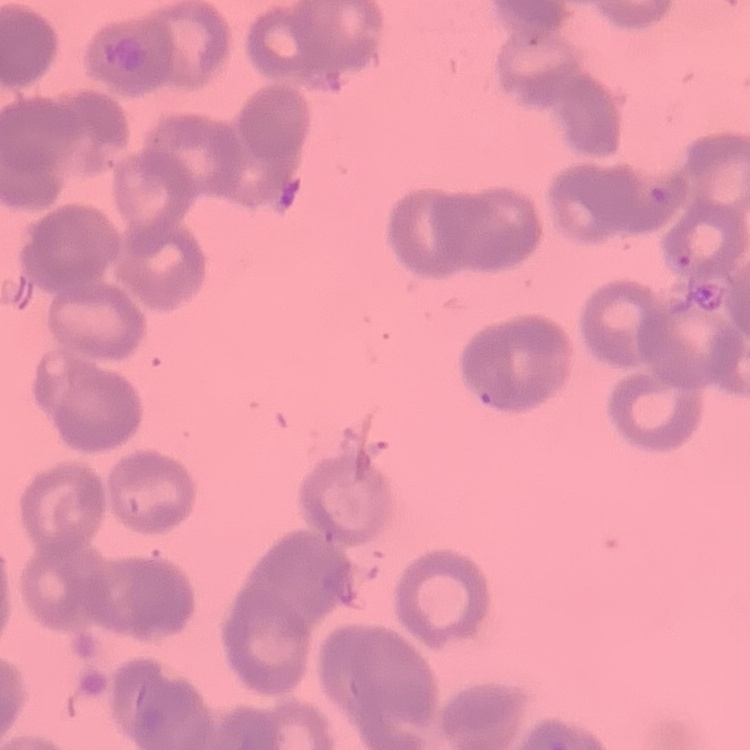

The red blood cells exhibit rouleaux formation. Thin blood smear. Field's or Giemsa stain. Square crop of a larger photomicrograph.